Comment on the morphology of the erythrocytes.
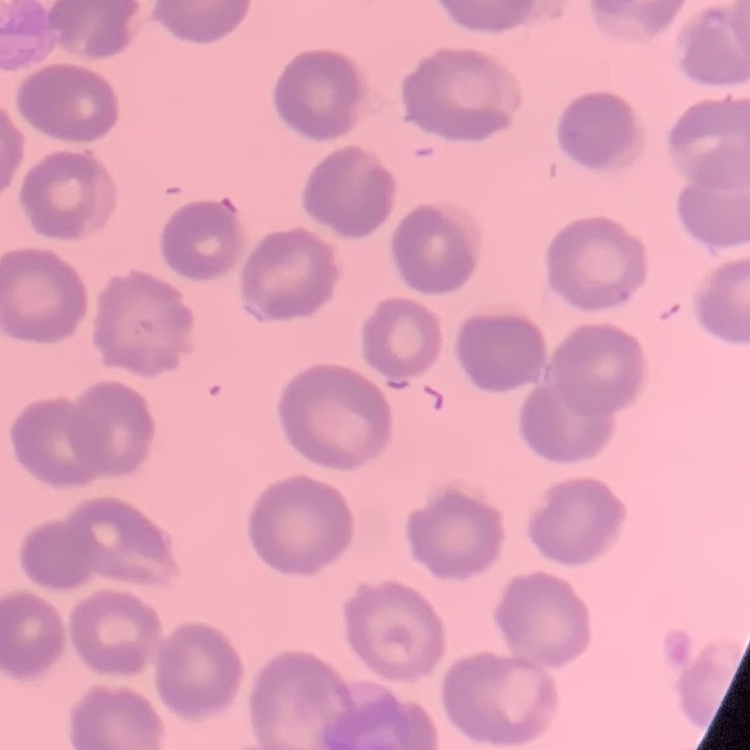
No rouleaux formation.

Thin blood smear. Square crop of a larger photomicrograph. Stained with either Field's or Giemsa.